Comment on the morphology of the erythrocytes.
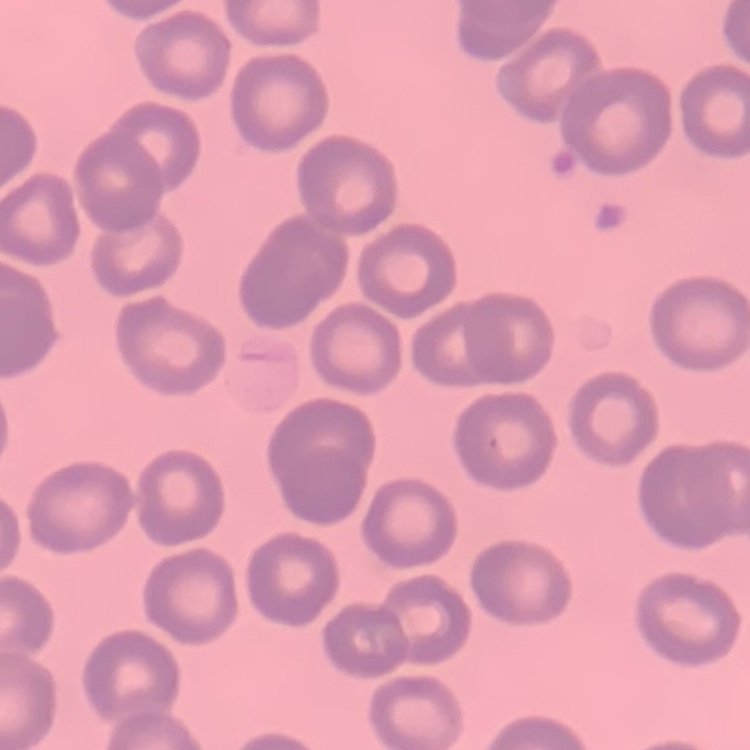
They show no rouleaux formation.

stain = Field's or Giemsa
preparation = thin blood smear
image type = square crop of a larger photomicrograph